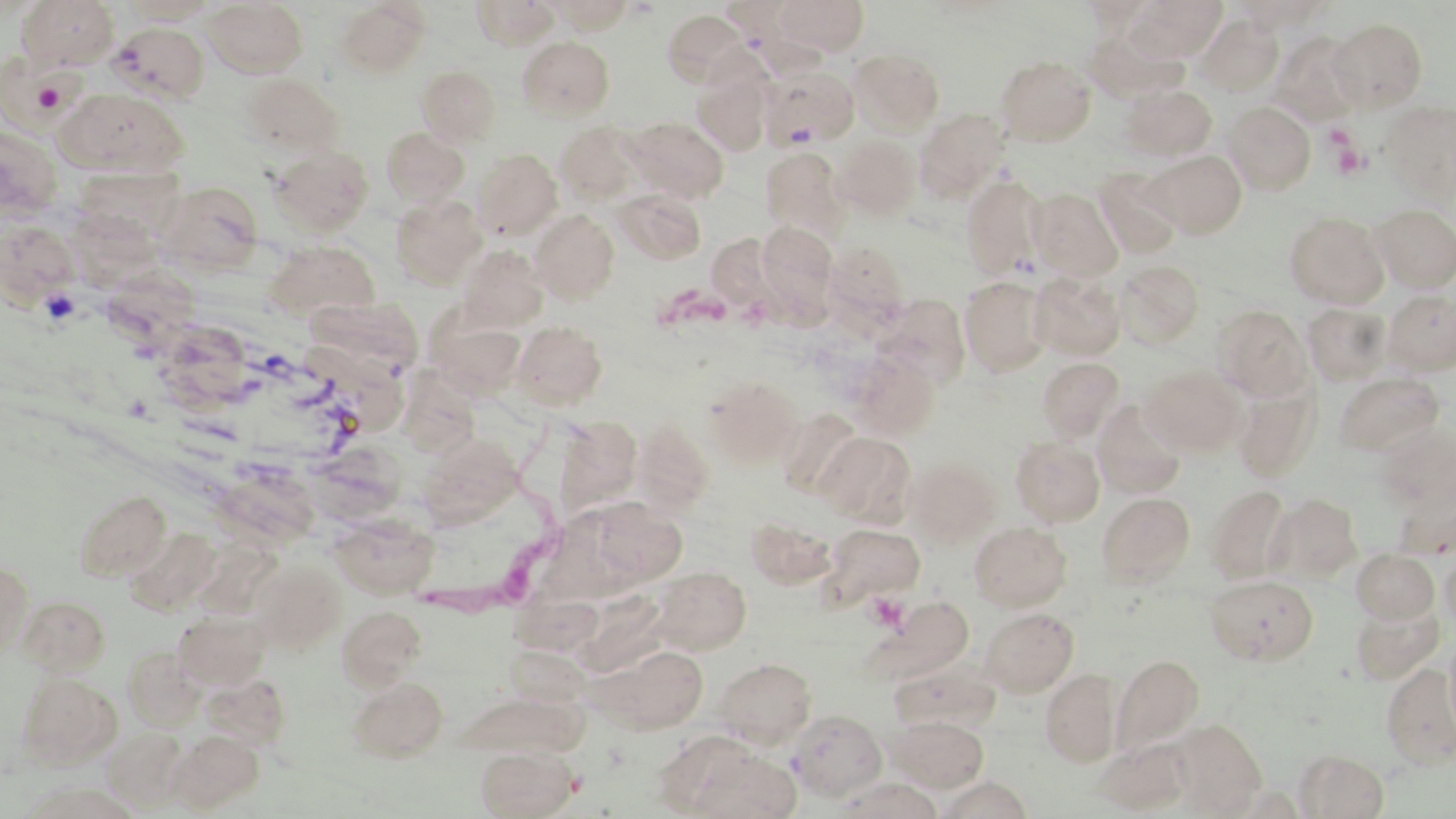 Approximate bounding boxes as named x1/y1/x2/y2 corners in pixels. Uninfected red blood cell locations: (x1=16, y1=0, x2=119, y2=70), (x1=471, y1=0, x2=560, y2=48), (x1=551, y1=0, x2=634, y2=32), (x1=776, y1=0, x2=870, y2=55), (x1=1079, y1=0, x2=1158, y2=28), (x1=1130, y1=0, x2=1226, y2=61), (x1=121, y1=1, x2=219, y2=24), (x1=204, y1=1, x2=307, y2=77), (x1=335, y1=1, x2=431, y2=76), (x1=719, y1=1, x2=803, y2=47), (x1=1234, y1=1, x2=1332, y2=32), (x1=663, y1=9, x2=748, y2=86), (x1=1197, y1=14, x2=1283, y2=96), (x1=1329, y1=18, x2=1428, y2=111), (x1=110, y1=22, x2=209, y2=103), (x1=1083, y1=27, x2=1185, y2=103), (x1=1270, y1=32, x2=1366, y2=125), (x1=517, y1=36, x2=614, y2=121), (x1=849, y1=48, x2=945, y2=135), (x1=1, y1=55, x2=84, y2=136), (x1=996, y1=55, x2=1095, y2=145), (x1=417, y1=65, x2=500, y2=146), (x1=760, y1=67, x2=858, y2=150), (x1=694, y1=71, x2=771, y2=155), (x1=240, y1=73, x2=344, y2=157), (x1=1119, y1=84, x2=1217, y2=160), (x1=57, y1=88, x2=188, y2=178), (x1=1224, y1=101, x2=1316, y2=194), (x1=1379, y1=102, x2=1456, y2=203), (x1=915, y1=109, x2=1009, y2=201), (x1=625, y1=117, x2=729, y2=203), (x1=555, y1=122, x2=643, y2=204), (x1=0, y1=125, x2=63, y2=221), (x1=381, y1=127, x2=469, y2=207), (x1=834, y1=135, x2=920, y2=219), (x1=269, y1=144, x2=374, y2=236), (x1=760, y1=146, x2=848, y2=240), (x1=473, y1=148, x2=563, y2=240), (x1=1146, y1=150, x2=1247, y2=238), (x1=71, y1=166, x2=188, y2=251), (x1=1094, y1=168, x2=1184, y2=259), (x1=961, y1=175, x2=1047, y2=279), (x1=156, y1=180, x2=264, y2=274), (x1=613, y1=188, x2=706, y2=265), (x1=1028, y1=188, x2=1123, y2=281), (x1=390, y1=194, x2=486, y2=289), (x1=1370, y1=204, x2=1456, y2=292), (x1=530, y1=209, x2=620, y2=303), (x1=1284, y1=211, x2=1389, y2=309), (x1=0, y1=219, x2=79, y2=306), (x1=757, y1=222, x2=837, y2=306), (x1=706, y1=233, x2=772, y2=308), (x1=264, y1=240, x2=380, y2=321), (x1=825, y1=243, x2=910, y2=322), (x1=458, y1=245, x2=549, y2=331), (x1=1116, y1=259, x2=1204, y2=349), (x1=100, y1=265, x2=204, y2=352), (x1=1029, y1=271, x2=1126, y2=361), (x1=960, y1=276, x2=1052, y2=376), (x1=1384, y1=288, x2=1456, y2=375), (x1=309, y1=297, x2=423, y2=380), (x1=1302, y1=303, x2=1392, y2=386), (x1=1212, y1=304, x2=1312, y2=401), (x1=154, y1=318, x2=256, y2=411), (x1=430, y1=318, x2=527, y2=399), (x1=512, y1=321, x2=608, y2=410), (x1=849, y1=349, x2=941, y2=441), (x1=1037, y1=357, x2=1124, y2=441), (x1=1142, y1=365, x2=1246, y2=456), (x1=1334, y1=371, x2=1444, y2=457), (x1=704, y1=375, x2=803, y2=468), (x1=402, y1=377, x2=480, y2=462), (x1=1233, y1=384, x2=1321, y2=483), (x1=1092, y1=399, x2=1187, y2=500), (x1=776, y1=408, x2=864, y2=498), (x1=632, y1=419, x2=715, y2=514), (x1=559, y1=421, x2=645, y2=514), (x1=1375, y1=423, x2=1456, y2=511), (x1=816, y1=432, x2=916, y2=527), (x1=422, y1=434, x2=523, y2=533), (x1=314, y1=435, x2=409, y2=521), (x1=1010, y1=436, x2=1105, y2=526), (x1=906, y1=456, x2=1002, y2=547), (x1=205, y1=470, x2=322, y2=554), (x1=1205, y1=484, x2=1292, y2=584), (x1=74, y1=489, x2=171, y2=581), (x1=1097, y1=492, x2=1195, y2=588), (x1=598, y1=493, x2=692, y2=589), (x1=1265, y1=493, x2=1362, y2=582), (x1=554, y1=509, x2=634, y2=605), (x1=329, y1=510, x2=440, y2=599), (x1=745, y1=514, x2=837, y2=589), (x1=969, y1=521, x2=1071, y2=611), (x1=821, y1=523, x2=925, y2=604), (x1=125, y1=527, x2=220, y2=614), (x1=1351, y1=549, x2=1440, y2=624), (x1=1440, y1=549, x2=1456, y2=632), (x1=0, y1=558, x2=34, y2=658), (x1=248, y1=558, x2=347, y2=654), (x1=651, y1=566, x2=751, y2=654), (x1=1205, y1=574, x2=1318, y2=666), (x1=515, y1=585, x2=606, y2=659), (x1=16, y1=594, x2=111, y2=675), (x1=874, y1=595, x2=973, y2=682), (x1=1351, y1=600, x2=1444, y2=684), (x1=337, y1=605, x2=427, y2=689), (x1=980, y1=607, x2=1079, y2=696), (x1=173, y1=610, x2=270, y2=690), (x1=1444, y1=634, x2=1456, y2=744), (x1=593, y1=643, x2=709, y2=733), (x1=121, y1=644, x2=205, y2=732), (x1=507, y1=649, x2=601, y2=713), (x1=1111, y1=653, x2=1204, y2=757), (x1=715, y1=657, x2=816, y2=749), (x1=890, y1=663, x2=998, y2=734), (x1=1380, y1=663, x2=1456, y2=769), (x1=1041, y1=669, x2=1123, y2=768), (x1=15, y1=670, x2=120, y2=769), (x1=201, y1=671, x2=291, y2=752), (x1=348, y1=676, x2=448, y2=762), (x1=452, y1=691, x2=594, y2=763), (x1=789, y1=710, x2=887, y2=800), (x1=887, y1=716, x2=988, y2=793), (x1=1170, y1=720, x2=1266, y2=816), (x1=102, y1=728, x2=188, y2=810), (x1=168, y1=730, x2=264, y2=812), (x1=1096, y1=738, x2=1194, y2=814), (x1=676, y1=740, x2=802, y2=819), (x1=475, y1=745, x2=577, y2=819), (x1=1297, y1=749, x2=1389, y2=818), (x1=937, y1=776, x2=1032, y2=818), (x1=832, y1=777, x2=942, y2=818), (x1=19, y1=781, x2=141, y2=819). Platelet locations: (x1=29, y1=73, x2=73, y2=116), (x1=1322, y1=124, x2=1357, y2=154), (x1=1331, y1=141, x2=1370, y2=180), (x1=866, y1=592, x2=909, y2=632). Trypanosoma brucei locations: (x1=413, y1=424, x2=568, y2=631). Slide-level diagnosis: Trypanosoma brucei. Optical microscopy. 1000x magnification. Thin blood smear. May-Grünwald-Giemsa stain. Image is 1456×819 pixels. One field of a larger specimen.